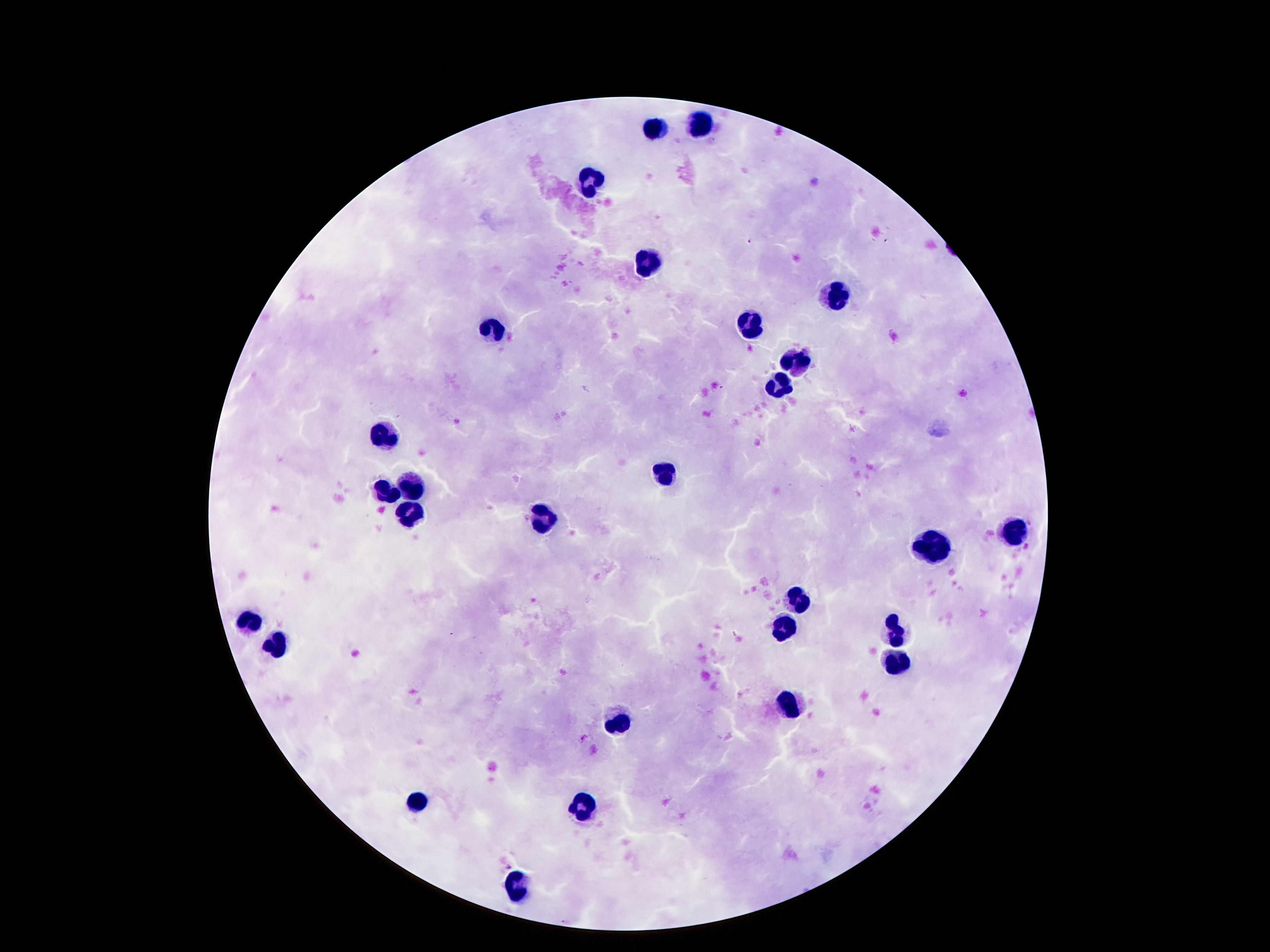

Approximate centers as [x, y] in pixels.
Summary:
  - Leukocyte locations: [699, 122], [658, 128], [593, 180], [645, 262], [837, 295], [749, 325], [490, 329], [798, 359], [774, 388], [385, 434], [664, 474], [413, 480], [387, 491], [411, 516], [544, 519], [1011, 532], [934, 549], [796, 602], [779, 625], [899, 633], [895, 662], [789, 704], [622, 723], [419, 802], [583, 809], [512, 892]
  - Preparation: thick peripheral-blood smear
  - Capture: smartphone camera through the microscope eyepiece
  - Field of view: one from this slide
  - Image size: 1270×952 pixels
  - Magnification: 100x
  - Patient malaria status: negative
  - Stain: Giemsa